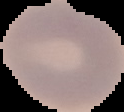
image size = 124×112 pixels
image type = segmented cell region with the area outside set to black
preparation = thin blood smear
malaria status = uninfected